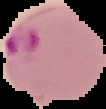

Summary:
  - Image size: 106×109 pixels
  - Malaria status: parasitized
  - Image type: cell region segmented out of the field of view; surrounding area masked to black
  - Preparation: thin blood smear